Point out each Plasmodium parasite.
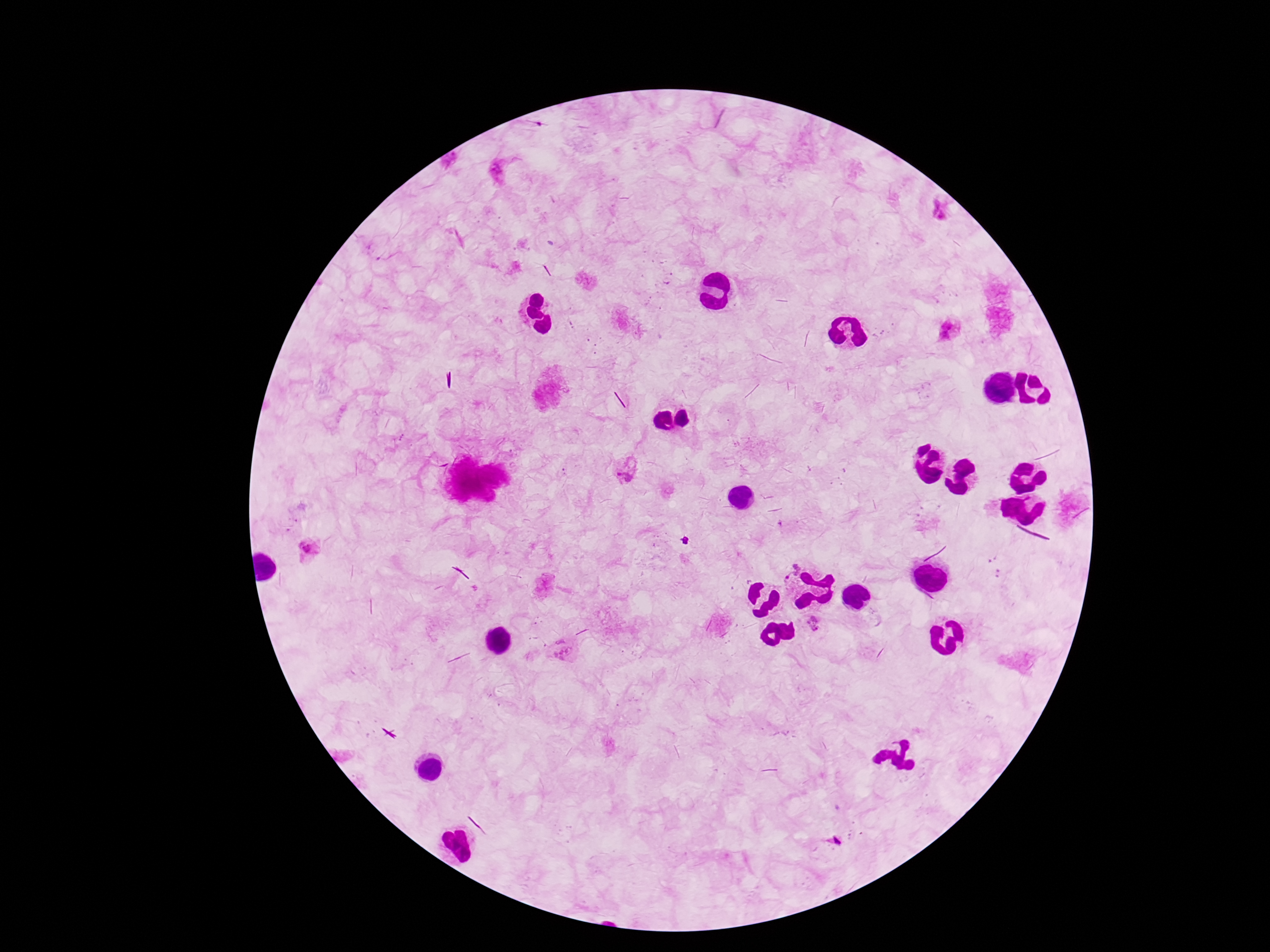

Approximate object centers, in pixels from the top-left corner.
Plasmodium parasites: (x=451, y=160), (x=502, y=169), (x=942, y=211), (x=949, y=329), (x=627, y=470), (x=310, y=550), (x=788, y=569), (x=815, y=624), (x=561, y=648).

Summary:
  - Patient malaria status: positive
  - Preparation: thick blood smear
  - Image size: 1270×952 pixels
  - Magnification: 100x
  - Field of view: one from this slide
  - Capture: smartphone camera through the microscope eyepiece
  - Stain: Giemsa